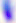
{
  "identification": "Toxoplasma gondii",
  "magnification": "400x",
  "modality": "micrograph"
}